Describe the morphology of the erythrocytes.
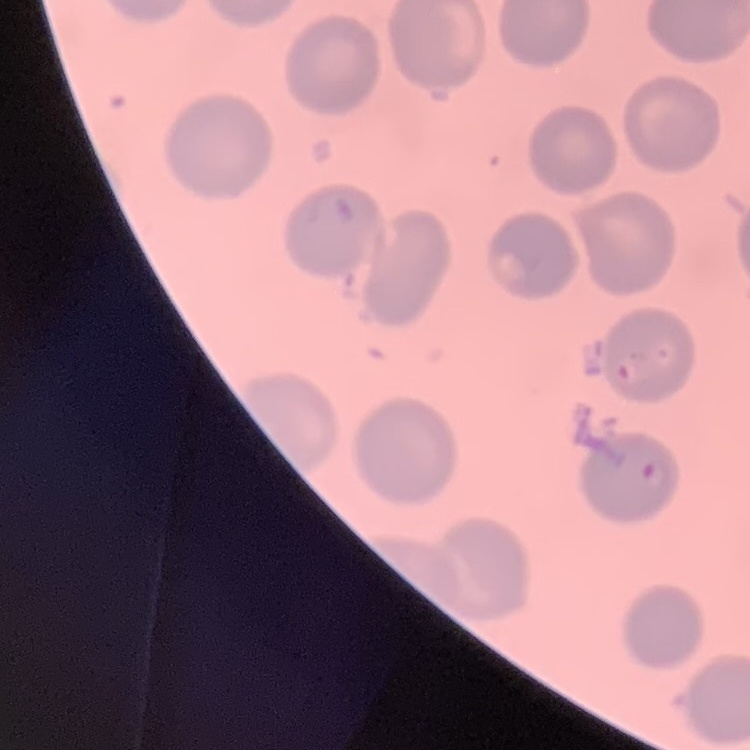
They show no rouleaux formation.

Field's or Giemsa stain. Thin blood smear. One tile cut from a larger photomicrograph.